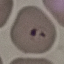
Summary:
  - Malaria status: parasitized
  - Preparation: thin smear
  - Capture: smartphone through the microscope eyepiece
  - Stain: Giemsa
  - Image type: automatically extracted cell patch, resized to 64 × 64 pixels